Assess for Plasmodium parasites.
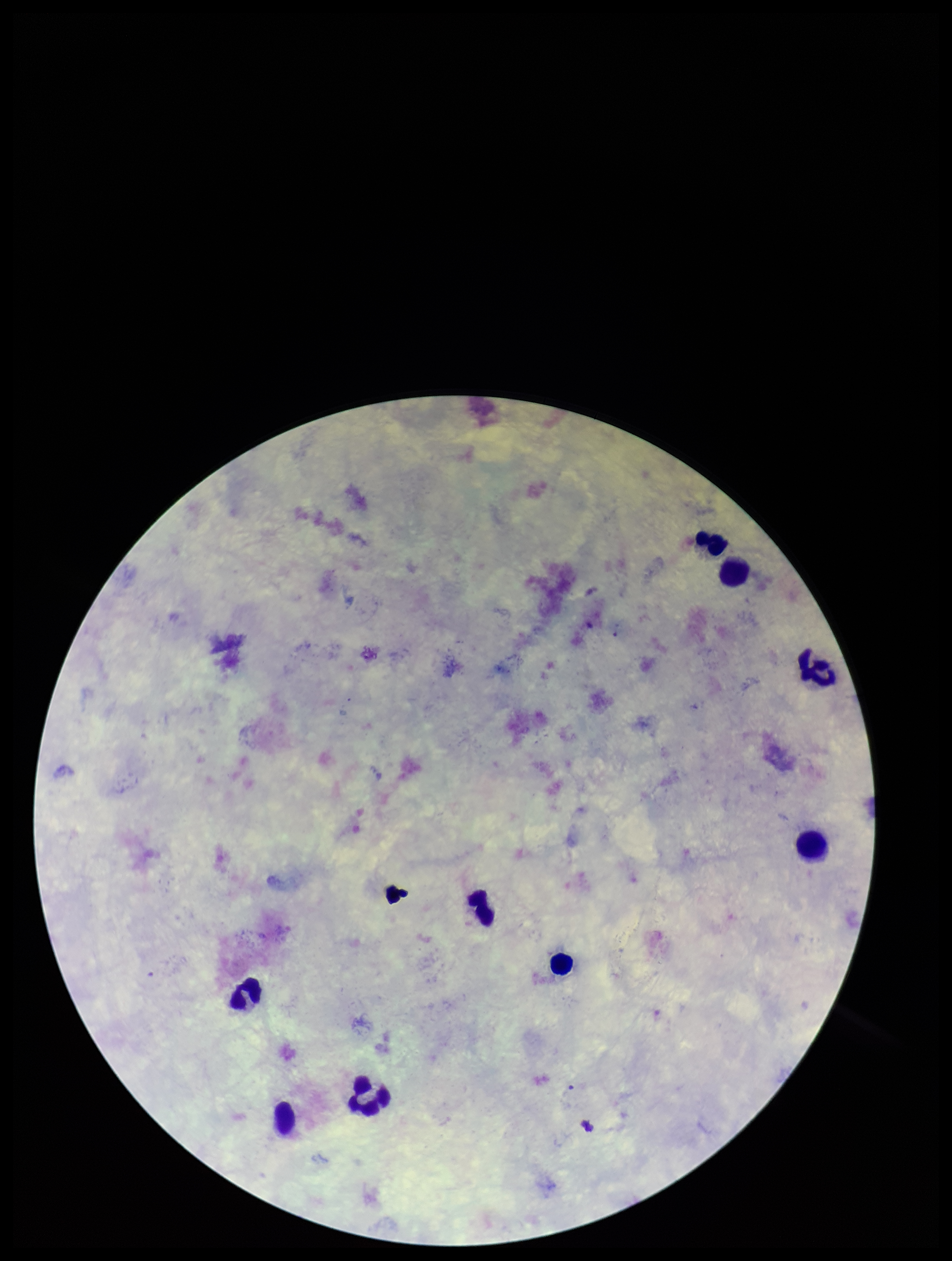
None detected.

capture = smartphone photograph through the microscope eyepiece
stain = Giemsa
field of view = one from this slide
image size = 952×1261 pixels
parasite count = 0
preparation = thick
leukocyte count = 9
patient malaria status = negative